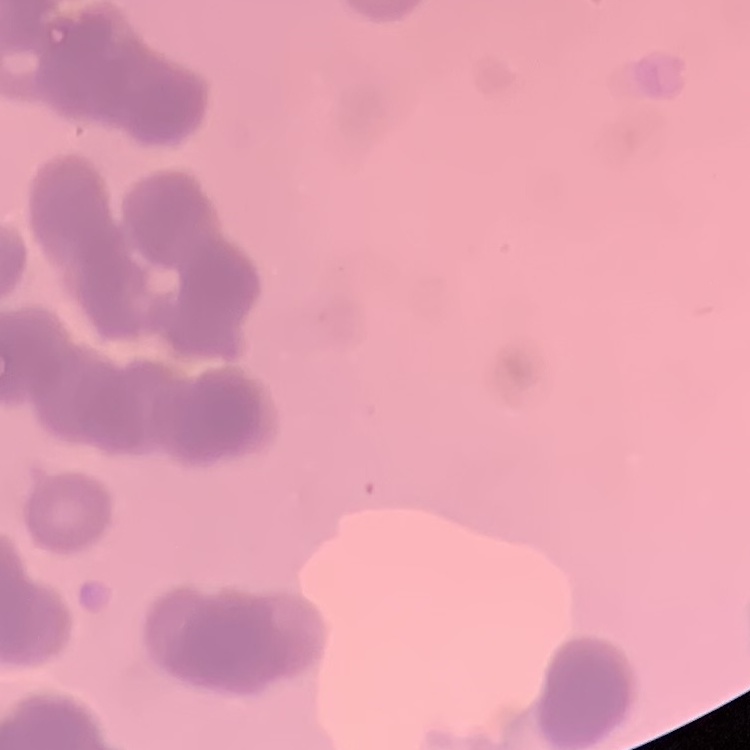

The red blood cells exhibit rouleaux formation. Thin blood film. Square crop of a larger photomicrograph. Stained with either Field's or Giemsa.